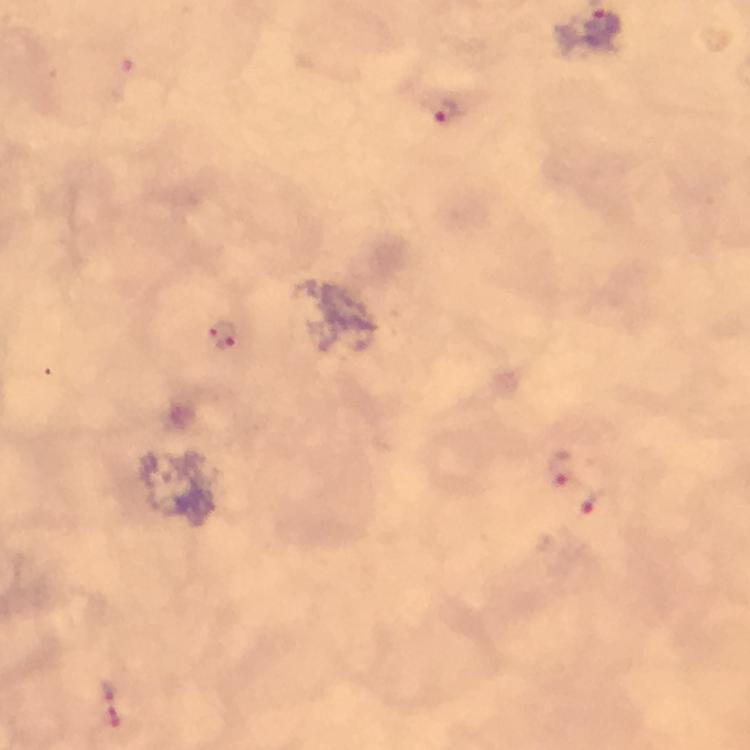
Approximate object centers, in pixels from the top-left corner.
Summary:
  - Plasmodium parasite locations: (x=442, y=109), (x=222, y=336), (x=562, y=467), (x=596, y=501), (x=110, y=702)
  - Capture: smartphone photograph through a microscope
  - Immersion oil: used
  - Stain: Giemsa
  - Magnification: 100x
  - Cropped from: one field of view
  - Preparation: thick blood smear
  - Image size: 750×750 pixels
  - Context: from a diagnostic examination for malaria